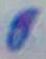
Photomicrograph. 1000x magnification. Toxoplasma gondii is shown.